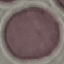
Malaria status: uninfected. Thin smear of blood. Acquired by smartphone through the microscope eyepiece. Automatically extracted cell patch, resized to 64 × 64 pixels. Giemsa-stained preparation.